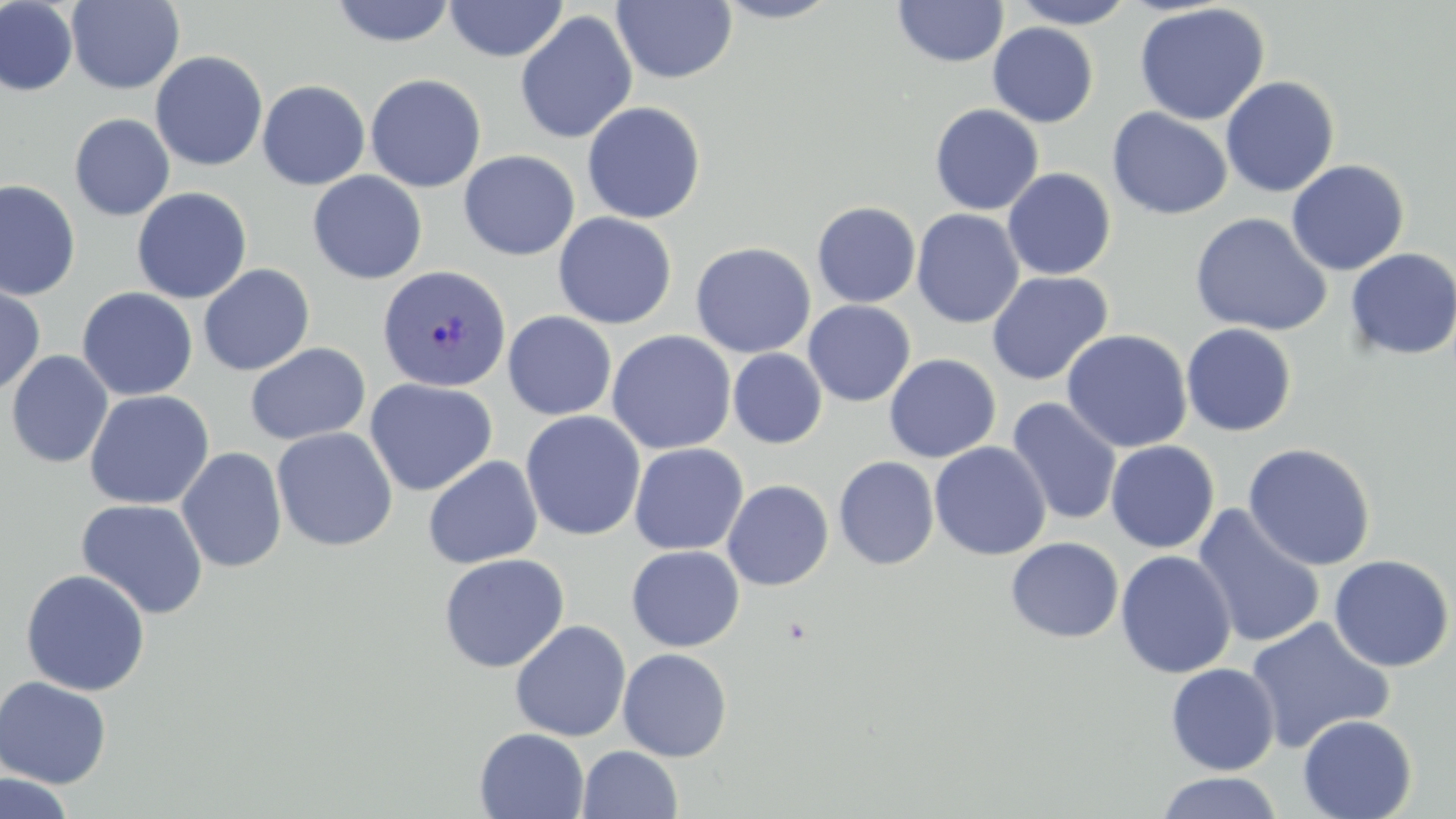
slide_level_diagnosis: Plasmodium vivax
magnification: 1000x
uninfected_red_blood_cell_locations: 'approximate bounding boxes as named x1/y1/x2/y2 corners in pixels: (x1=612, y1=0, x2=737, y2=84), (x1=711, y1=0, x2=844, y2=24), (x1=893, y1=0, x2=1009, y2=67), (x1=1009, y1=0, x2=1137, y2=28), (x1=0, y1=1, x2=78, y2=97), (x1=66, y1=1, x2=184, y2=94), (x1=329, y1=1, x2=458, y2=47), (x1=445, y1=1, x2=567, y2=62), (x1=1134, y1=3, x2=1270, y2=125), (x1=515, y1=10, x2=638, y2=145), (x1=987, y1=22, x2=1099, y2=127), (x1=150, y1=51, x2=268, y2=172), (x1=365, y1=73, x2=486, y2=192), (x1=1219, y1=76, x2=1340, y2=197), (x1=257, y1=79, x2=371, y2=190), (x1=582, y1=101, x2=706, y2=224), (x1=929, y1=103, x2=1044, y2=215), (x1=1107, y1=107, x2=1233, y2=220), (x1=69, y1=113, x2=175, y2=221), (x1=459, y1=150, x2=580, y2=260), (x1=1286, y1=159, x2=1410, y2=276), (x1=1002, y1=167, x2=1116, y2=280), (x1=308, y1=171, x2=427, y2=284), (x1=0, y1=180, x2=81, y2=300), (x1=131, y1=188, x2=252, y2=304), (x1=812, y1=202, x2=921, y2=307), (x1=911, y1=209, x2=1024, y2=329), (x1=553, y1=212, x2=677, y2=329), (x1=1189, y1=212, x2=1332, y2=337), (x1=690, y1=242, x2=816, y2=358), (x1=1344, y1=248, x2=1456, y2=360), (x1=198, y1=263, x2=315, y2=376), (x1=986, y1=270, x2=1114, y2=386), (x1=0, y1=283, x2=45, y2=397), (x1=77, y1=287, x2=198, y2=401), (x1=803, y1=300, x2=916, y2=406), (x1=502, y1=311, x2=617, y2=420), (x1=1181, y1=323, x2=1297, y2=437), (x1=606, y1=330, x2=736, y2=454), (x1=1062, y1=330, x2=1192, y2=452), (x1=245, y1=342, x2=371, y2=446), (x1=728, y1=348, x2=827, y2=448), (x1=5, y1=350, x2=113, y2=469), (x1=884, y1=353, x2=1001, y2=463), (x1=364, y1=378, x2=498, y2=497), (x1=83, y1=390, x2=214, y2=509), (x1=1006, y1=398, x2=1122, y2=526), (x1=521, y1=411, x2=646, y2=542), (x1=271, y1=426, x2=398, y2=552), (x1=1105, y1=440, x2=1220, y2=553), (x1=929, y1=441, x2=1051, y2=561), (x1=629, y1=442, x2=748, y2=555), (x1=1242, y1=442, x2=1377, y2=571), (x1=176, y1=447, x2=288, y2=573), (x1=423, y1=455, x2=543, y2=569), (x1=834, y1=456, x2=940, y2=570), (x1=721, y1=479, x2=834, y2=591), (x1=75, y1=498, x2=209, y2=619), (x1=1191, y1=505, x2=1326, y2=649), (x1=1006, y1=537, x2=1124, y2=643), (x1=626, y1=545, x2=745, y2=651), (x1=1115, y1=550, x2=1236, y2=678), (x1=438, y1=552, x2=570, y2=672), (x1=1328, y1=554, x2=1455, y2=672), (x1=20, y1=568, x2=151, y2=696), (x1=1245, y1=617, x2=1395, y2=753), (x1=509, y1=620, x2=631, y2=742), (x1=617, y1=648, x2=733, y2=762), (x1=1165, y1=662, x2=1280, y2=775), (x1=0, y1=675, x2=113, y2=789), (x1=1297, y1=714, x2=1417, y2=819), (x1=474, y1=728, x2=590, y2=818), (x1=578, y1=745, x2=683, y2=819), (x1=1156, y1=771, x2=1284, y2=819), (x1=0, y1=772, x2=75, y2=818)'
image_size: 1456×819 pixels
modality: optical microscopy
field_of_view: single
stain: May-Grünwald-Giemsa
plasmodium_vivax_infected_red_blood_cell_locations: 'approximate bounding boxes as named x1/y1/x2/y2 corners in pixels: (x1=377, y1=264, x2=512, y2=392)'
preparation: thin blood film